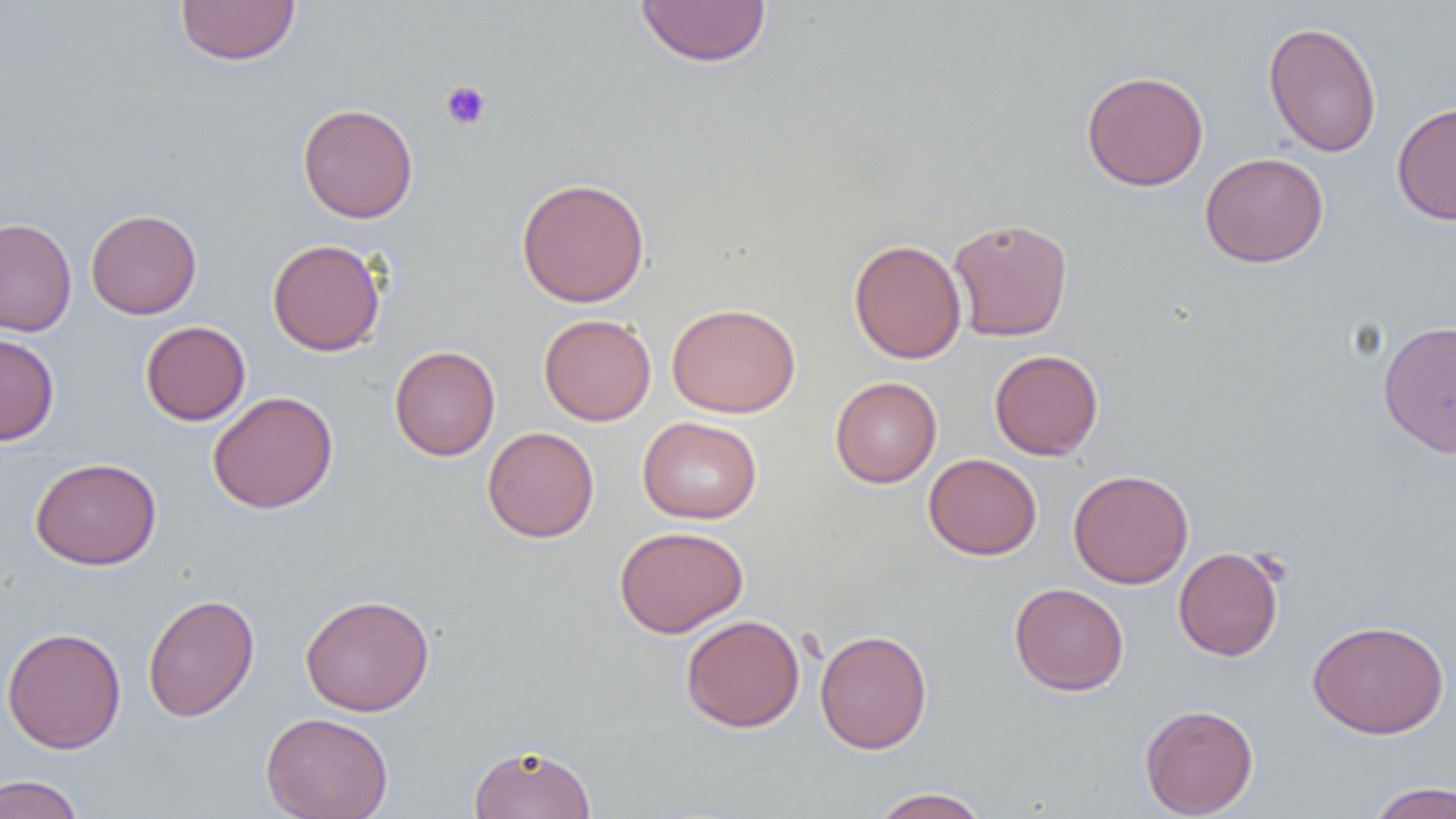
Approximate bounding boxes as (x1,y1)-(x2,y2) corner pairs in pixels. Uninfected red blood cell locations: (175,0)-(301,66), (635,0)-(772,68), (1263,20)-(1382,157), (1081,70)-(1209,191), (1391,101)-(1456,225), (297,103)-(418,224), (1200,152)-(1329,268), (516,177)-(650,308), (86,208)-(201,319), (0,217)-(77,336), (947,217)-(1073,342), (267,238)-(386,356), (849,238)-(967,364), (666,302)-(801,418), (539,313)-(656,426), (1377,319)-(1456,458), (140,321)-(250,425), (0,333)-(59,445), (389,345)-(501,461), (989,349)-(1104,461), (830,376)-(942,488), (208,391)-(338,514), (637,416)-(762,524), (482,426)-(599,543), (923,453)-(1042,560), (30,457)-(161,571), (1068,469)-(1194,589), (614,525)-(748,638), (1173,546)-(1285,661), (1009,582)-(1129,696), (142,593)-(259,722), (299,594)-(435,716), (680,614)-(805,733), (1307,619)-(1449,739), (1,626)-(126,754), (814,628)-(932,754), (1139,703)-(1258,818), (261,712)-(393,819), (469,742)-(597,819), (0,774)-(85,819), (1365,781)-(1456,819), (870,787)-(990,818). Platelet locations: (440,80)-(492,130). Slide-level diagnosis: negative for blood parasites. Optical microscopy. One field of a larger specimen. Thin blood smear. Captured at 1000x magnification. Image is 1456×819 pixels.